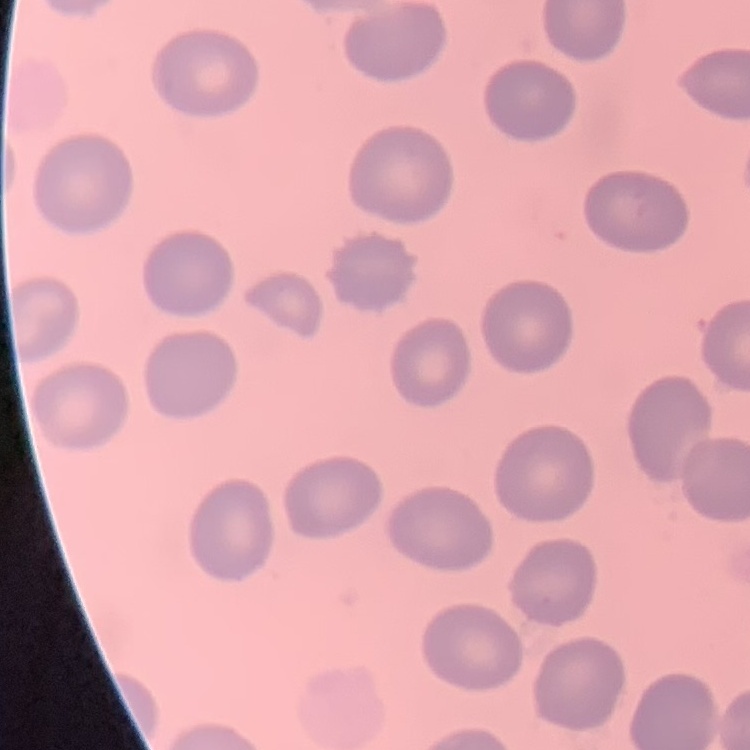

red blood cell morphology = no rouleaux formation
image type = one tile cut from a larger photomicrograph
stain = Field's or Giemsa
preparation = thin peripheral smear